Point out each malaria parasite.
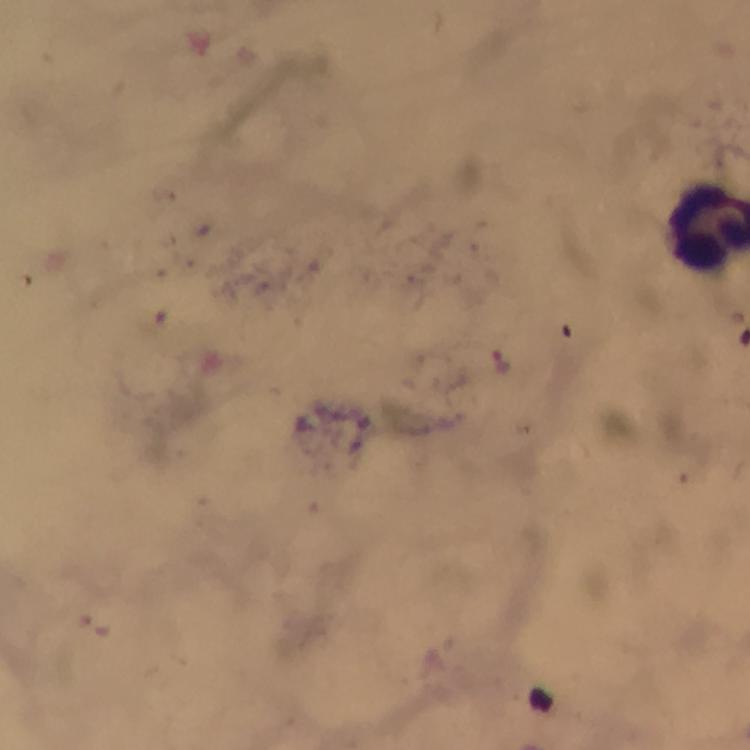
Approximate centers as (x, y) in pixels.
Malaria parasites: (502, 360).

Thick smear. Photographed with a smartphone mounted on the microscope. Image is 750×750 pixels. Giemsa stain. At 100x magnification. A crop from one field of view. From a malaria diagnostic workup. Immersion oil was used.